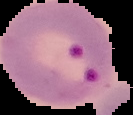

From a thin blood smear. Image is 133×115 pixels. Result: malaria parasites detected. Segmented cell region on a black background.